Give the position of every leukocyte visible.
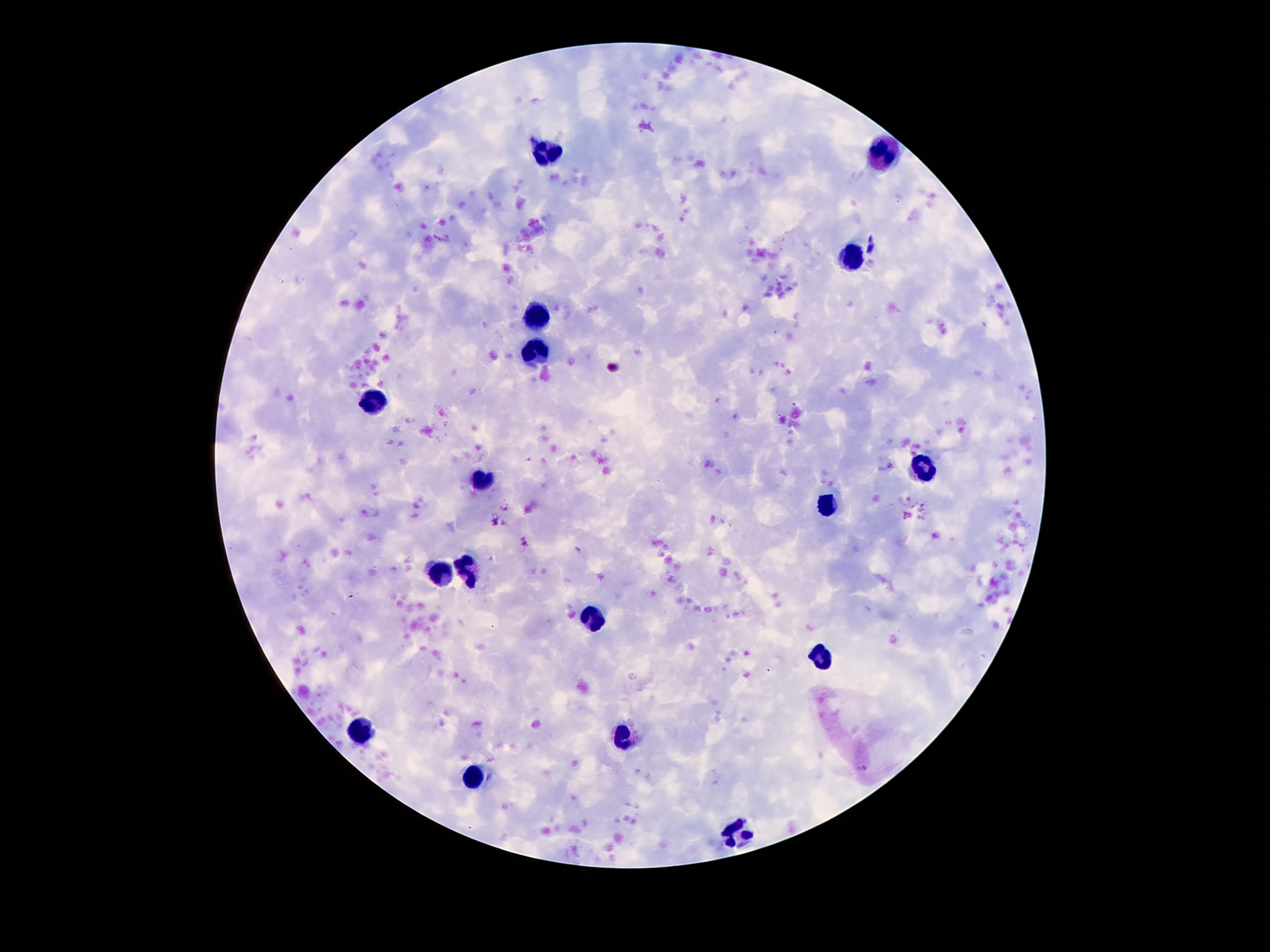

Approximate centers as {x, y} in pixels.
Leukocytes: {543, 152}, {886, 154}, {849, 260}, {534, 315}, {536, 352}, {372, 402}, {924, 469}, {481, 483}, {827, 506}, {466, 570}, {440, 574}, {592, 619}, {820, 654}, {359, 731}, {620, 738}, {474, 778}, {736, 833}.

Patient malaria status: negative. Giemsa stain. Smartphone photograph taken through the microscope eyepiece. 100x magnification. Thick peripheral-blood smear. One field from this slide. Image is 1270×952 pixels.